Locate every Plasmodium parasite and every leukocyte.
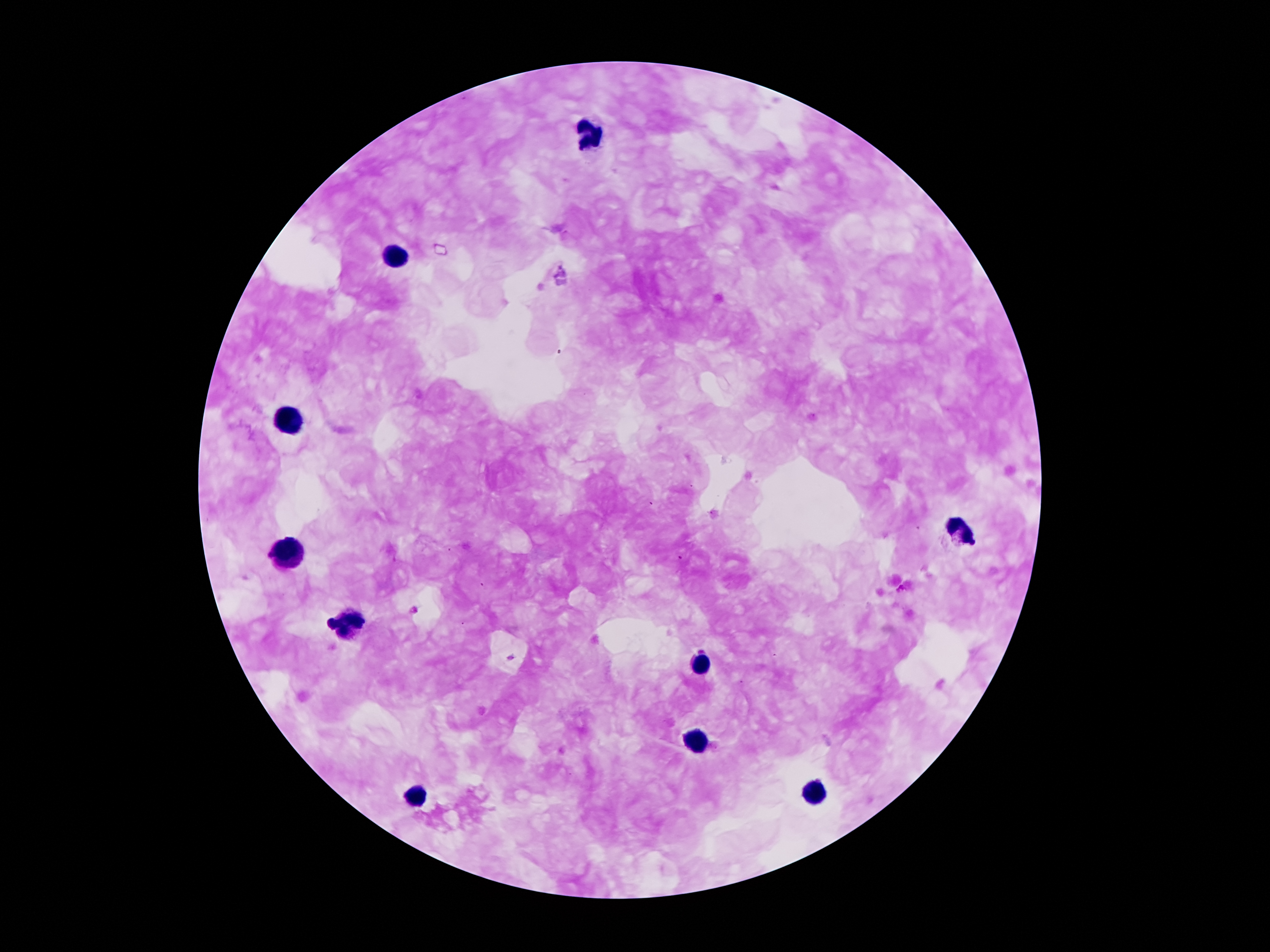

Approximate centers as [x, y] in pixels.
Plasmodium parasites: [680, 557].
Leukocytes: [586, 133], [397, 257], [290, 421], [960, 532], [288, 553], [342, 625], [699, 666], [694, 743], [815, 794], [415, 797].

Thick peripheral-blood smear. One field from this slide. Giemsa stain. Smartphone photograph taken through the microscope eyepiece. 100x magnification. Patient malaria status: infected with Plasmodium falciparum. Image is 1270×952 pixels.